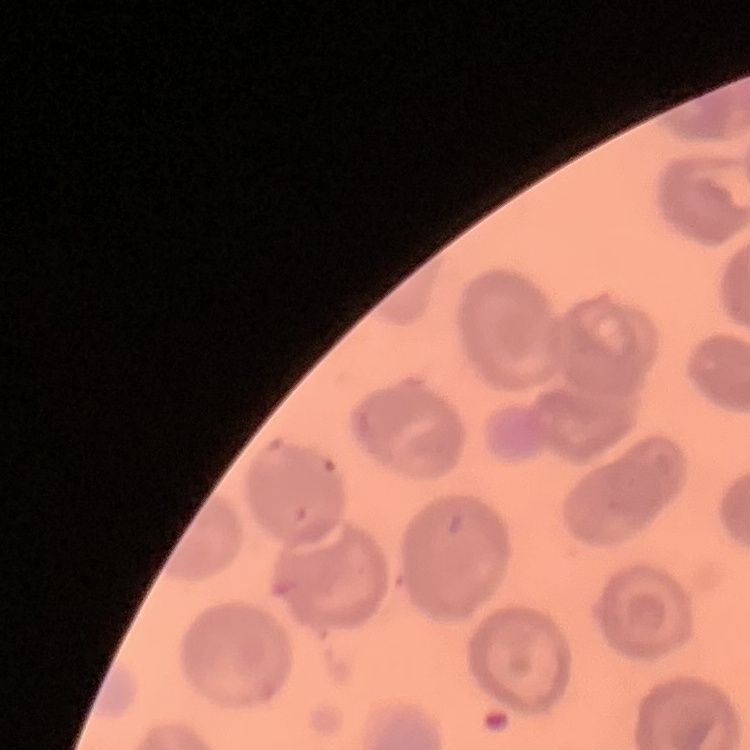
Summary:
  - Erythrocyte morphology: no rouleaux formation
  - Image type: square crop of a larger photomicrograph
  - Preparation: thin blood film
  - Stain: Field's or Giemsa